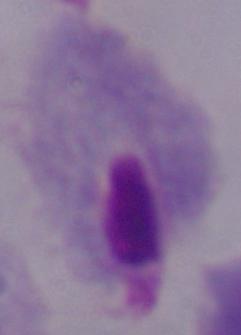

magnification = 1000x
identification = trichomonad
modality = micrograph